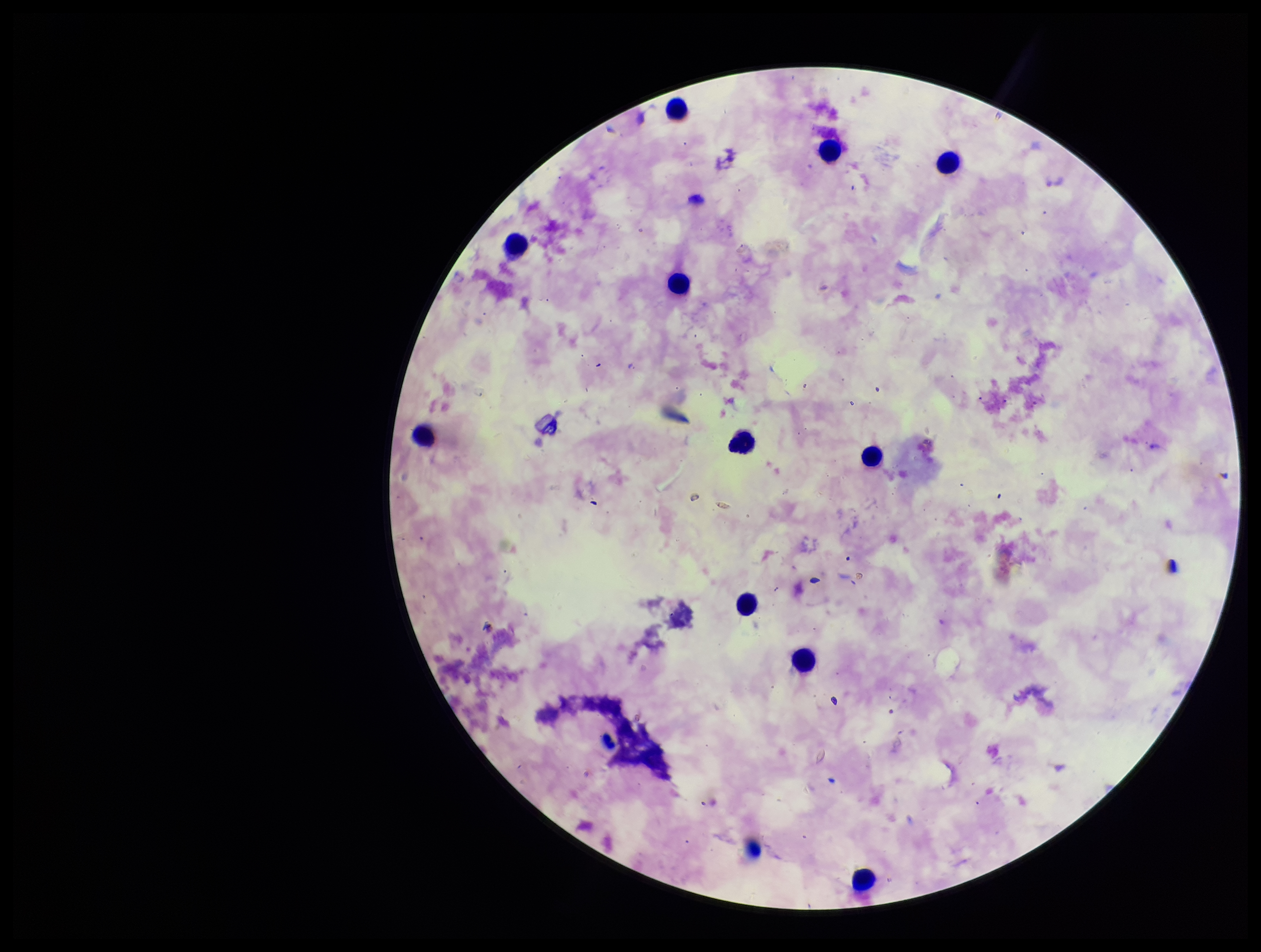
Summary:
  - Preparation: thick
  - Stain: Giemsa
  - Patient malaria status: infected
  - Image size: 1261×952 pixels
  - Capture: smartphone photograph through the microscope eyepiece
  - Parasite count: 0
  - Plasmodium parasites: none identified
  - Species reported for this patient: Plasmodium falciparum
  - Field of view: one from this slide
  - Leukocyte count: 12